Locate every Plasmodium vivax-infected red blood cell.
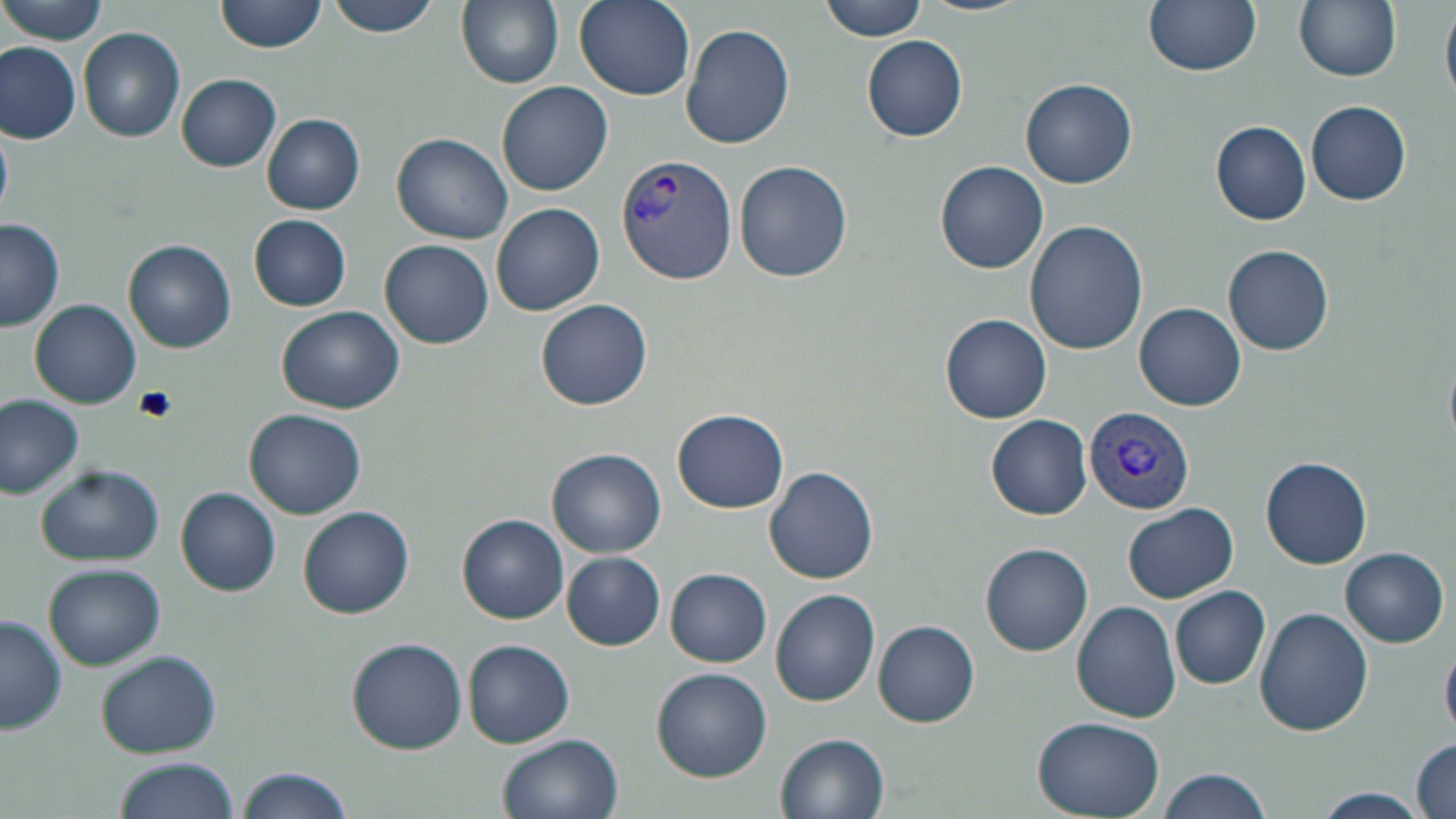
Approximate bounding boxes as named x1/y1/x2/y2 corners in pixels.
Plasmodium vivax-infected red blood cells: (x1=617, y1=152, x2=740, y2=282), (x1=1084, y1=405, x2=1193, y2=516).

Summary:
  - Uninfected red blood cell locations: (x1=2, y1=0, x2=109, y2=45), (x1=215, y1=0, x2=325, y2=53), (x1=322, y1=0, x2=444, y2=38), (x1=457, y1=0, x2=563, y2=89), (x1=574, y1=0, x2=695, y2=100), (x1=820, y1=0, x2=927, y2=41), (x1=917, y1=0, x2=1029, y2=16), (x1=1144, y1=0, x2=1261, y2=74), (x1=1294, y1=0, x2=1401, y2=83), (x1=1442, y1=0, x2=1456, y2=109), (x1=681, y1=25, x2=795, y2=149), (x1=78, y1=27, x2=185, y2=144), (x1=861, y1=35, x2=969, y2=141), (x1=1, y1=41, x2=81, y2=143), (x1=177, y1=74, x2=281, y2=172), (x1=1021, y1=76, x2=1137, y2=188), (x1=497, y1=81, x2=613, y2=197), (x1=1305, y1=100, x2=1412, y2=205), (x1=263, y1=113, x2=365, y2=215), (x1=1210, y1=120, x2=1311, y2=224), (x1=0, y1=126, x2=14, y2=218), (x1=391, y1=133, x2=513, y2=244), (x1=734, y1=160, x2=853, y2=282), (x1=936, y1=160, x2=1048, y2=273), (x1=491, y1=203, x2=604, y2=316), (x1=247, y1=214, x2=352, y2=311), (x1=0, y1=220, x2=63, y2=330), (x1=1025, y1=221, x2=1148, y2=356), (x1=380, y1=238, x2=493, y2=348), (x1=124, y1=240, x2=237, y2=354), (x1=1224, y1=244, x2=1334, y2=355), (x1=30, y1=298, x2=142, y2=407), (x1=537, y1=298, x2=652, y2=409), (x1=1136, y1=301, x2=1246, y2=412), (x1=278, y1=307, x2=402, y2=413), (x1=940, y1=314, x2=1052, y2=422), (x1=0, y1=396, x2=84, y2=500), (x1=245, y1=407, x2=366, y2=517), (x1=673, y1=407, x2=788, y2=513), (x1=987, y1=415, x2=1092, y2=520), (x1=548, y1=448, x2=667, y2=558), (x1=1260, y1=457, x2=1372, y2=568), (x1=35, y1=464, x2=165, y2=566), (x1=764, y1=465, x2=882, y2=583), (x1=176, y1=487, x2=281, y2=596), (x1=1123, y1=503, x2=1239, y2=603), (x1=298, y1=506, x2=415, y2=619), (x1=458, y1=514, x2=570, y2=623), (x1=979, y1=542, x2=1094, y2=656), (x1=1341, y1=547, x2=1448, y2=646), (x1=1009, y1=551, x2=1146, y2=673), (x1=563, y1=552, x2=666, y2=650), (x1=44, y1=562, x2=165, y2=669), (x1=666, y1=568, x2=771, y2=666), (x1=1170, y1=586, x2=1271, y2=689), (x1=771, y1=589, x2=879, y2=708), (x1=1071, y1=600, x2=1181, y2=723), (x1=1254, y1=605, x2=1374, y2=736), (x1=0, y1=614, x2=67, y2=734), (x1=872, y1=619, x2=980, y2=727), (x1=346, y1=637, x2=467, y2=754), (x1=1441, y1=637, x2=1456, y2=741), (x1=463, y1=639, x2=575, y2=747), (x1=95, y1=650, x2=221, y2=758), (x1=652, y1=667, x2=772, y2=781), (x1=1032, y1=715, x2=1165, y2=818), (x1=777, y1=733, x2=891, y2=819), (x1=497, y1=734, x2=622, y2=819), (x1=1412, y1=737, x2=1455, y2=819), (x1=112, y1=756, x2=240, y2=819), (x1=236, y1=766, x2=356, y2=819), (x1=1155, y1=767, x2=1272, y2=819), (x1=1308, y1=786, x2=1434, y2=816)
  - Platelet locations: (x1=135, y1=386, x2=178, y2=422)
  - Slide-level diagnosis: Plasmodium vivax
  - Magnification: 1000x
  - Field of view: one of a larger specimen
  - Image size: 1456×819 pixels
  - Stain: May-Grünwald-Giemsa
  - Preparation: thin blood smear
  - Modality: optical microscopy